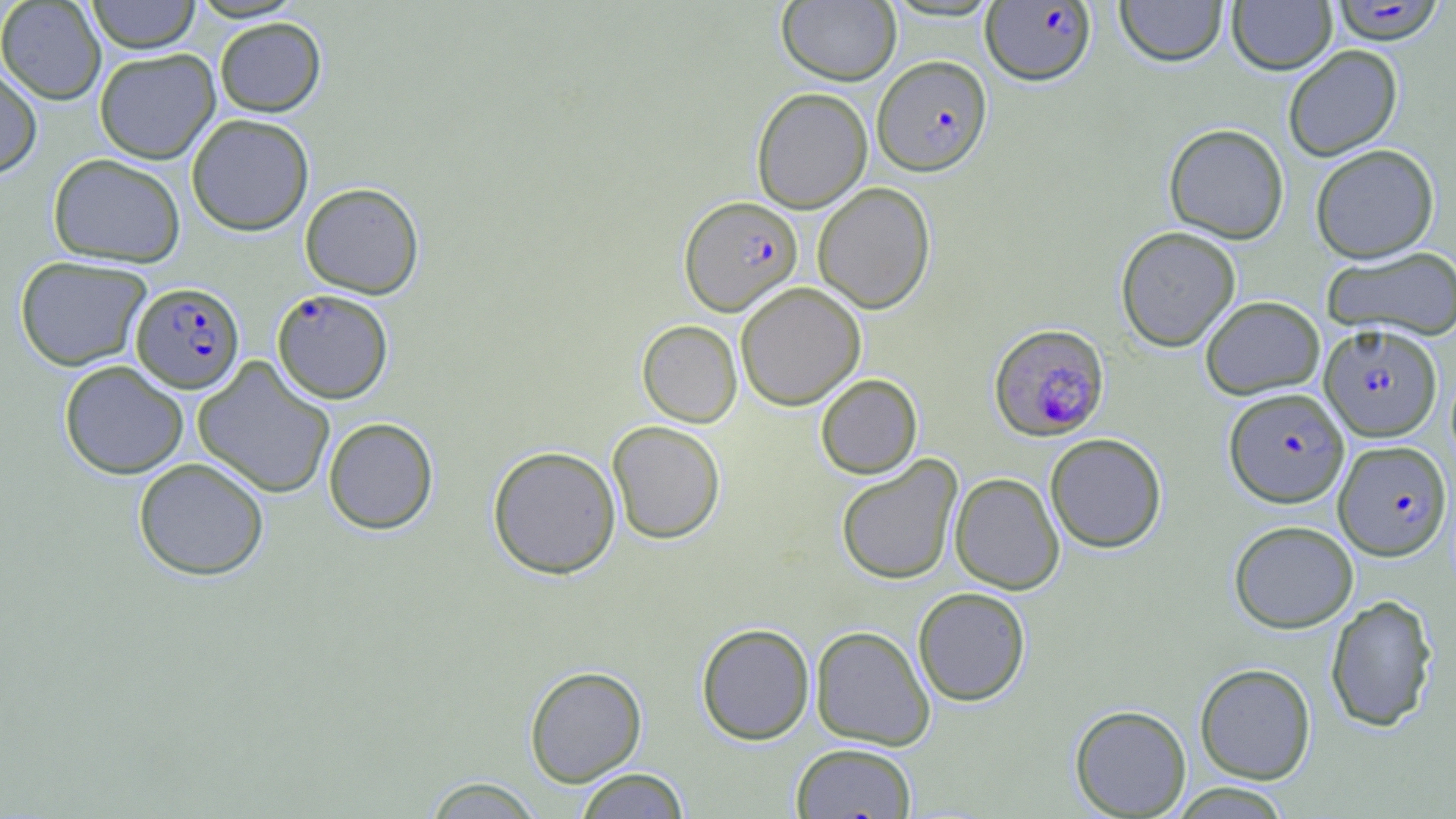
Approximate bounding boxes as [x1, y1, x2, y2] in pixels. Uninfected red blood cell locations: [0, 0, 106, 105], [86, 0, 201, 53], [777, 0, 901, 85], [1115, 0, 1227, 66], [1227, 0, 1336, 75], [214, 17, 326, 117], [1283, 45, 1403, 161], [94, 48, 221, 164], [0, 64, 42, 179], [751, 87, 872, 213], [187, 114, 314, 235], [1164, 123, 1289, 243], [1310, 144, 1439, 263], [48, 153, 186, 268], [299, 182, 424, 298], [813, 182, 936, 314], [1116, 226, 1241, 351], [1322, 246, 1456, 341], [15, 255, 152, 371], [735, 282, 866, 411], [1200, 295, 1325, 399], [637, 319, 742, 427], [192, 357, 336, 499], [59, 360, 189, 479], [815, 374, 922, 478], [323, 417, 438, 534], [607, 420, 726, 544], [1045, 433, 1167, 553], [487, 445, 621, 579], [836, 455, 963, 585], [133, 456, 269, 581], [950, 472, 1065, 594], [1229, 520, 1359, 633], [913, 587, 1031, 706], [1325, 593, 1437, 732], [696, 623, 815, 745], [810, 625, 935, 750], [1194, 662, 1316, 784], [524, 665, 647, 786], [1069, 704, 1191, 818], [791, 743, 918, 819], [574, 768, 691, 818], [422, 776, 546, 818], [1167, 783, 1295, 818]. Plasmodium falciparum-infected red blood cell locations: [981, 1, 1096, 85], [1332, 1, 1443, 45], [873, 55, 992, 175], [679, 195, 803, 315], [131, 282, 245, 393], [272, 288, 394, 403], [989, 323, 1110, 440], [1319, 323, 1442, 441], [1224, 387, 1349, 508], [1333, 440, 1452, 559]. Slide-level diagnosis: Plasmodium falciparum. Single field of view. Thin blood smear. May-Grünwald-Giemsa stain. Light microscopy. Image is 1456×819 pixels. Captured at 1000x magnification.